Identify the parasite.
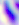

This is Toxoplasma gondii.

Summary:
  - Magnification: 400x
  - Modality: micrograph